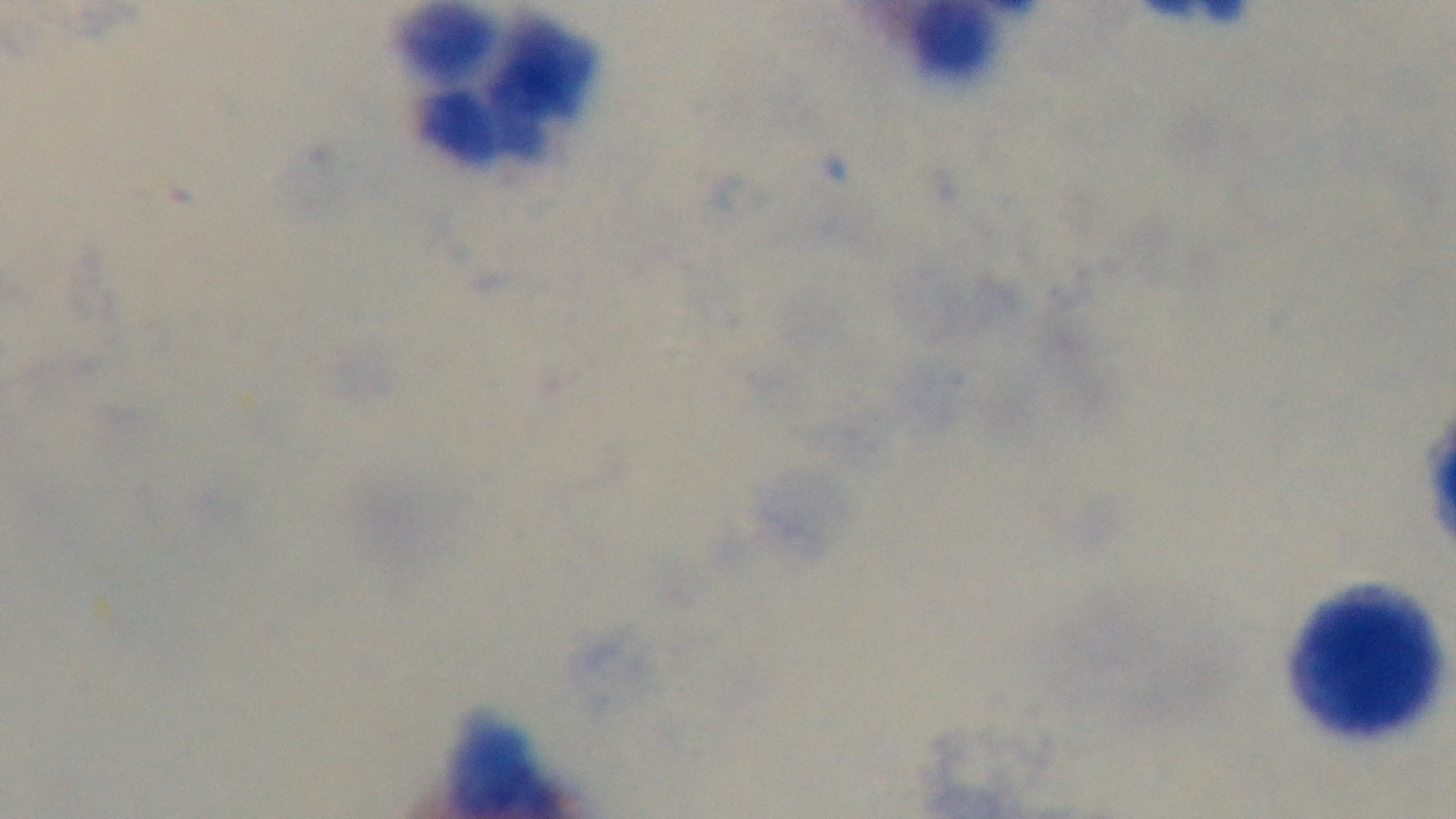
Summary:
  - Preparation: thick
  - Field of view: one from the slide
  - Malaria status: negative
  - Capture: mounted 4K digital camera
  - Modality: light microscopy
  - Objective: 100x oil immersion
  - Stain: Giemsa